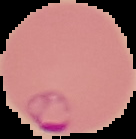

image type = cell region segmented out of the field of view; surrounding area masked to black
malaria status = parasitized
image size = 136×139 pixels
preparation = thin blood film